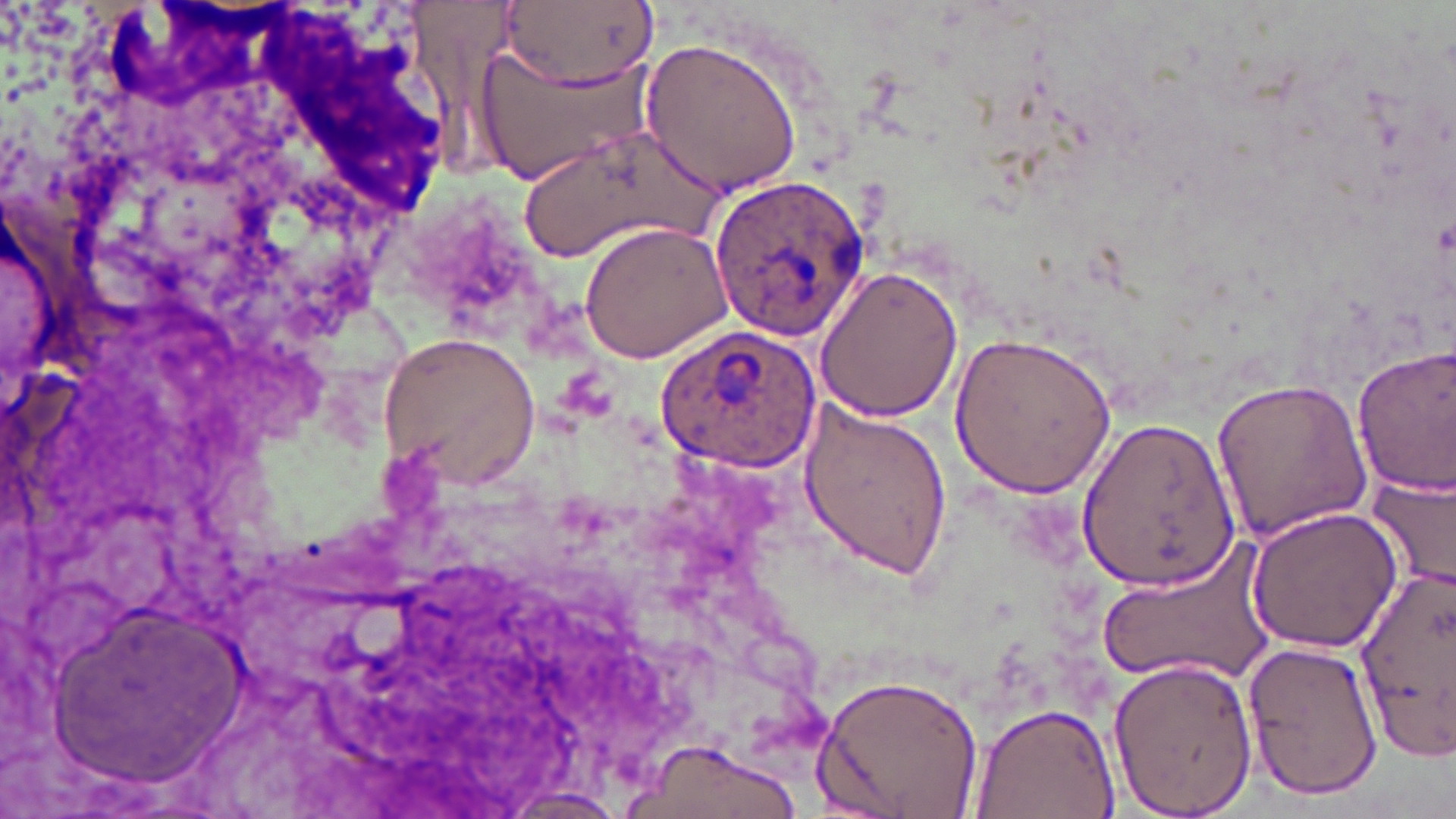
Approximate bounding boxes as (x1,y1)-(x2,y2) corner pairs in pixels. Plasmodium ovale-infected red blood cell locations: (710,176)-(875,339). Uninfected red blood cell locations: (497,0)-(657,93), (639,35)-(808,196), (472,47)-(658,187), (513,130)-(710,266), (577,220)-(733,363), (812,266)-(965,425), (656,326)-(823,473), (377,330)-(542,486), (949,331)-(1118,497), (1353,342)-(1456,499), (1209,376)-(1373,544), (795,399)-(954,582), (1078,414)-(1242,591), (1366,472)-(1456,593), (1244,505)-(1402,655), (1093,538)-(1275,688), (1356,557)-(1454,758), (48,594)-(240,792), (1242,640)-(1383,802), (1104,654)-(1258,819), (814,670)-(983,819), (972,701)-(1121,818), (632,740)-(798,819), (491,788)-(633,818). Slide-level diagnosis: Plasmodium ovale. One field of a larger specimen. Image is 1456×819 pixels. May-Grünwald-Giemsa-stained preparation. Captured at 1000x magnification. Thin blood film. Optical microscopy.